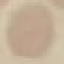
Result: negative for malaria parasites. Giemsa-stained preparation. Photographed with a smartphone camera at the microscope eyepiece. Cell patch, automatically extracted from a larger field of view and resized to 64 × 64 pixels. Thin smear of blood.